Classify this cell by malaria status.
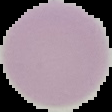
It is uninfected.

Summary:
  - Image size: 112×112 pixels
  - Image type: segmented cell region on a black background
  - Preparation: thin blood film